Comment on the morphology of the erythrocytes.
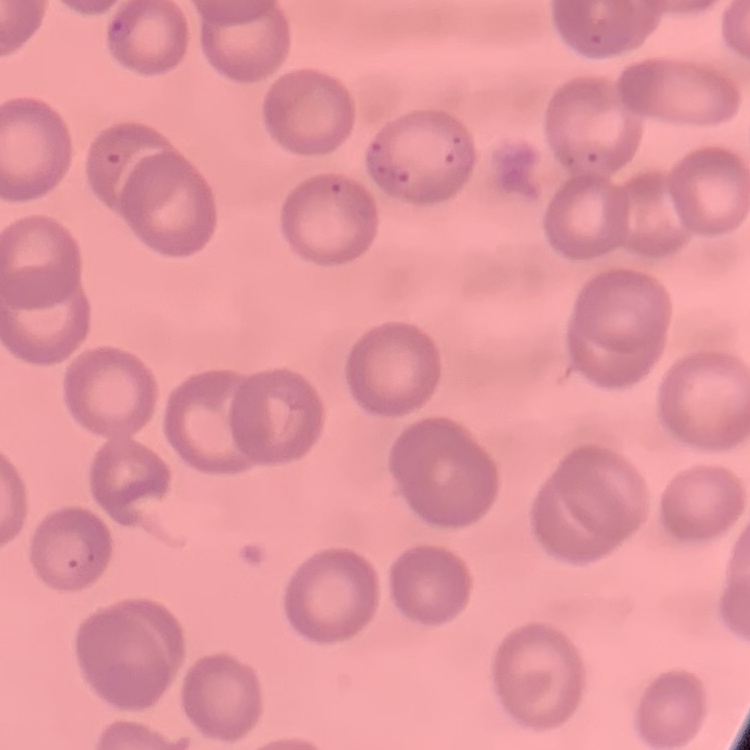
No rouleaux formation.

Thin peripheral smear. Field's or Giemsa stain. One tile cut from a larger photomicrograph.